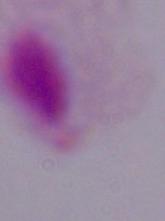
identification = trichomonad
magnification = 1000x
modality = micrograph